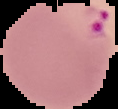
Segmented cell region on a black background. From a thin blood film. Malaria status: parasitized. Image is 118×109 pixels.